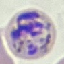
Summary:
  - Malaria status: parasitized
  - Stain: Giemsa
  - Preparation: thin smear
  - Image type: automatically extracted cell patch, resized to 64 × 64 pixels
  - Capture: smartphone camera at the microscope eyepiece